Find each WBC.
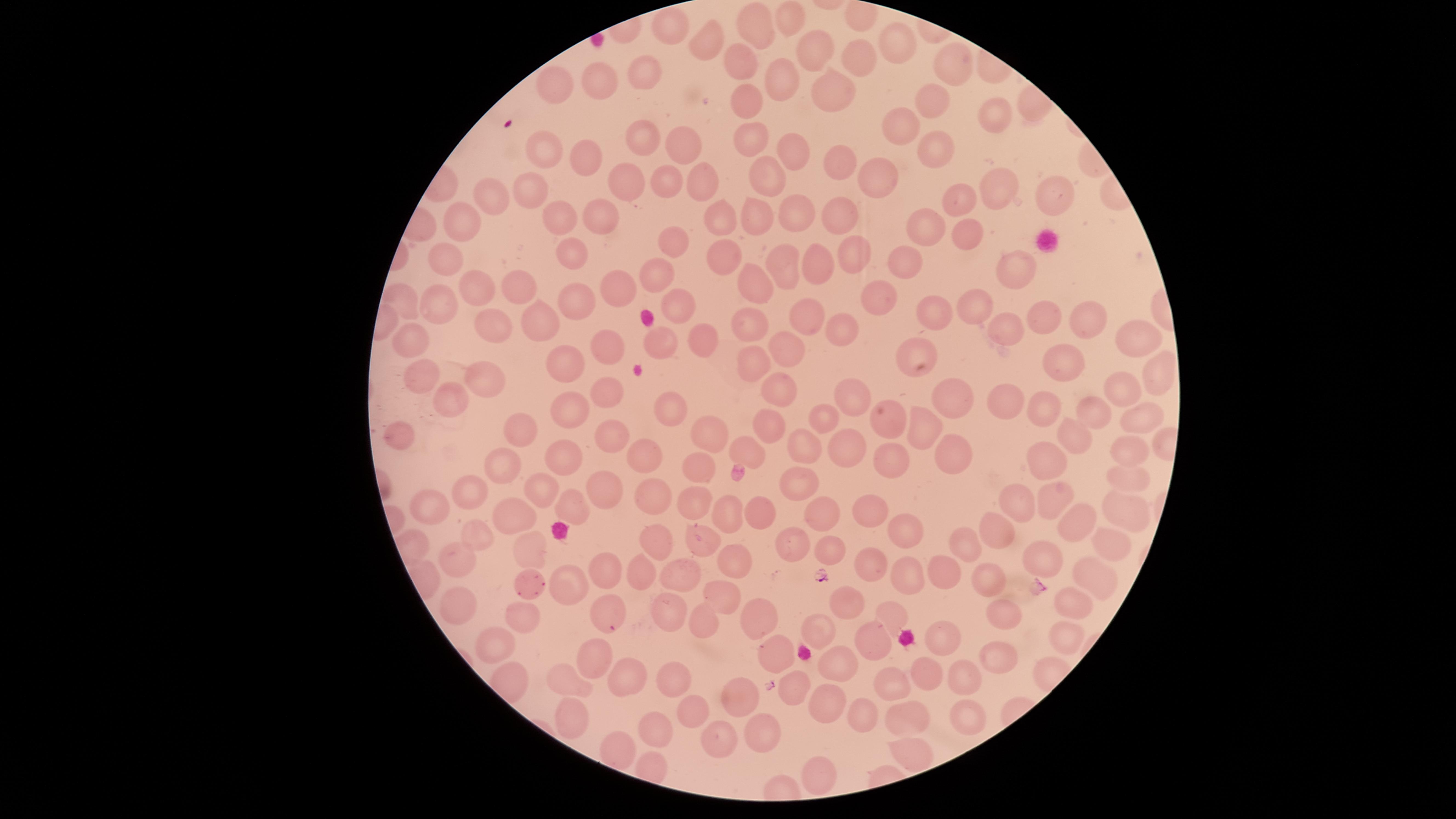
No WBCs identified.

capture: smartphone photograph through the microscope eyepiece
field_of_view: single
parasitized_RBCs: 'approximate marker points as [x, y] in pixels: [528, 582], [605, 614]'
species: Plasmodium falciparum
image_size: 1456×819 pixels
presence: malaria parasites detected
visible_region: circular
uninfected_RBCs: 'approximate marker points as [x, y] in pixels: [792, 19], [758, 24], [669, 25], [897, 42], [820, 48], [706, 54], [860, 58], [742, 59], [956, 62], [639, 70], [607, 79], [781, 79], [559, 84], [834, 93], [934, 100], [747, 101], [994, 117], [905, 125], [644, 133], [747, 138], [691, 141], [547, 147], [790, 150], [930, 153], [585, 159], [840, 166], [704, 176], [760, 176], [875, 178], [624, 179], [667, 179], [530, 180], [998, 189], [1051, 195], [485, 197], [959, 200], [800, 211], [556, 214], [595, 214], [759, 214], [721, 219], [845, 219], [464, 222], [922, 227], [967, 229], [671, 239], [447, 254], [576, 256], [855, 256], [719, 259], [779, 261], [811, 263], [907, 263], [1019, 265], [658, 275], [756, 281], [517, 286], [477, 287], [620, 289], [582, 296], [407, 299], [441, 299], [888, 299], [982, 301], [680, 307], [928, 309], [531, 315], [1050, 316], [805, 317], [492, 319], [1087, 322], [838, 328], [749, 329], [1006, 332], [1132, 334], [702, 340], [413, 342], [611, 343], [661, 343], [785, 348], [925, 354], [753, 361], [1072, 361], [562, 369], [1159, 369], [422, 373], [485, 379], [1127, 389], [604, 390], [447, 393], [782, 393], [849, 393], [950, 398], [1001, 400], [572, 401], [669, 402], [1048, 405], [1095, 410], [1144, 415], [825, 416], [895, 424], [768, 425], [521, 429], [922, 430], [714, 431], [612, 437], [1075, 438], [408, 439], [839, 446], [801, 449], [748, 453], [953, 454], [1127, 454], [565, 456], [1045, 459], [644, 460], [889, 466], [503, 469], [694, 469], [798, 481], [1122, 481], [544, 487], [598, 488], [468, 490], [652, 491], [1060, 496], [1017, 502], [570, 505], [691, 506], [875, 507], [438, 508], [1119, 513], [754, 514], [730, 515], [822, 515], [514, 519], [1078, 520], [997, 527], [908, 530], [476, 532], [656, 539], [791, 540], [706, 543], [970, 547], [1112, 547], [827, 548], [531, 551], [1047, 559], [466, 562], [873, 562], [737, 563], [946, 569], [606, 573], [681, 573], [903, 575], [1093, 576], [639, 577], [986, 581], [569, 586], [722, 589], [465, 599], [847, 601], [1072, 602], [675, 608], [758, 613], [1008, 614], [523, 615], [900, 616], [703, 623], [940, 629], [825, 634], [1062, 635], [864, 636], [500, 639], [777, 652], [996, 654], [594, 662], [839, 664], [970, 675], [927, 677], [631, 678], [890, 680], [570, 683], [679, 684], [793, 687], [743, 693], [824, 700], [695, 712], [967, 714], [569, 719], [863, 721], [908, 722], [764, 730], [659, 731], [731, 743], [914, 748], [622, 752], [815, 773]'
stain: Giemsa
preparation: thin smear of blood